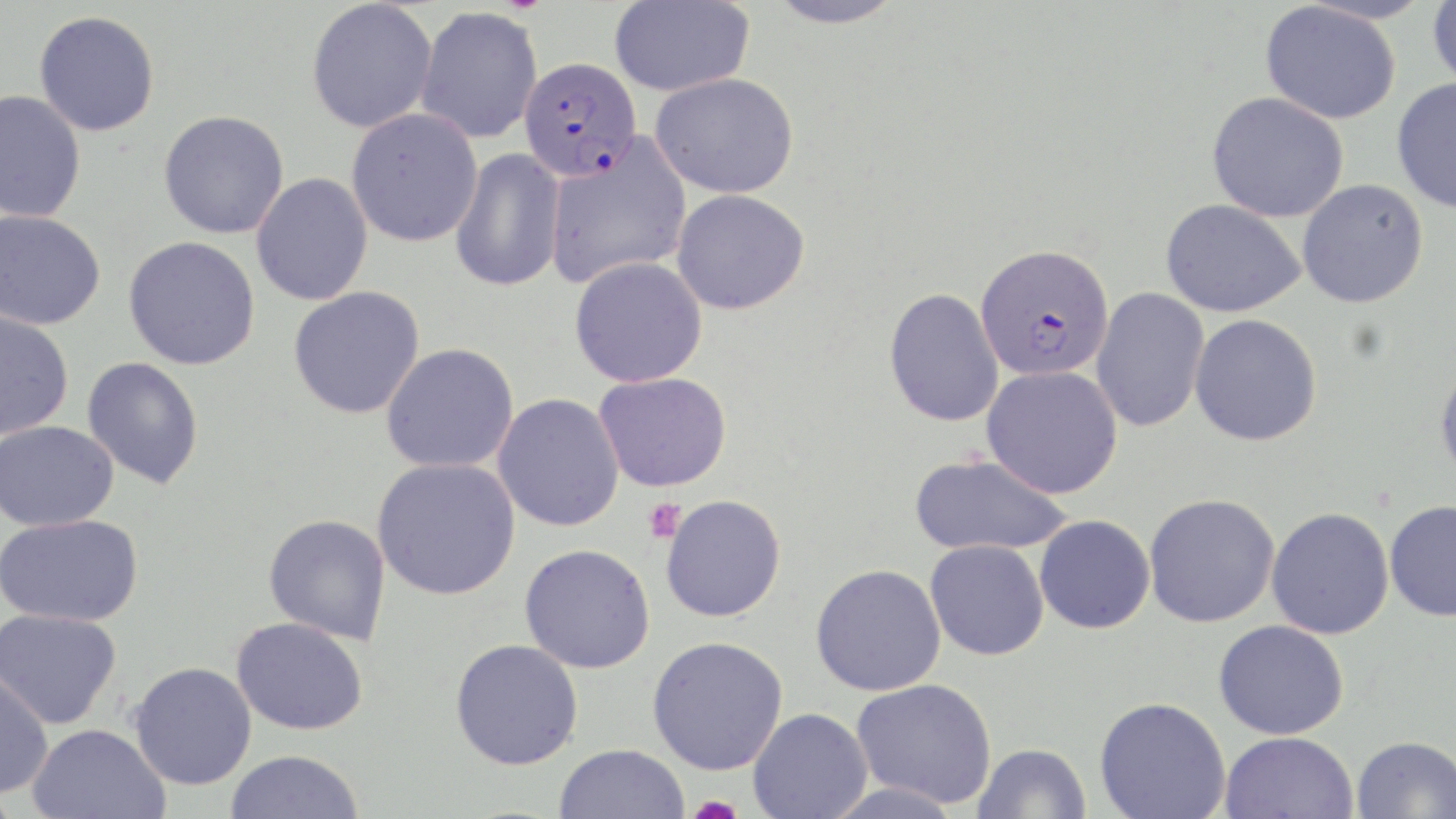 Approximate bounding boxes as named x1/y1/x2/y2 corners in pixels. Plasmodium falciparum-infected red blood cell locations: (x1=518, y1=56, x2=641, y2=181), (x1=975, y1=243, x2=1114, y2=381). Platelet locations: (x1=643, y1=498, x2=687, y2=543), (x1=684, y1=796, x2=746, y2=819). Uninfected red blood cell locations: (x1=306, y1=0, x2=438, y2=133), (x1=609, y1=0, x2=754, y2=96), (x1=764, y1=0, x2=907, y2=29), (x1=1427, y1=0, x2=1456, y2=93), (x1=1260, y1=2, x2=1401, y2=124), (x1=415, y1=6, x2=543, y2=144), (x1=33, y1=10, x2=160, y2=137), (x1=650, y1=72, x2=800, y2=198), (x1=1392, y1=77, x2=1456, y2=215), (x1=0, y1=90, x2=86, y2=222), (x1=1207, y1=92, x2=1349, y2=222), (x1=158, y1=109, x2=289, y2=239), (x1=346, y1=109, x2=483, y2=247), (x1=544, y1=136, x2=692, y2=289), (x1=449, y1=147, x2=566, y2=293), (x1=251, y1=173, x2=373, y2=306), (x1=1297, y1=178, x2=1429, y2=308), (x1=671, y1=189, x2=810, y2=315), (x1=1160, y1=199, x2=1306, y2=317), (x1=0, y1=210, x2=105, y2=330), (x1=122, y1=236, x2=261, y2=371), (x1=569, y1=257, x2=708, y2=387), (x1=288, y1=286, x2=426, y2=419), (x1=883, y1=287, x2=1004, y2=427), (x1=1091, y1=287, x2=1210, y2=433), (x1=0, y1=309, x2=74, y2=439), (x1=1189, y1=313, x2=1322, y2=446), (x1=381, y1=343, x2=519, y2=474), (x1=82, y1=356, x2=205, y2=490), (x1=1434, y1=360, x2=1456, y2=486), (x1=981, y1=365, x2=1123, y2=498), (x1=593, y1=371, x2=732, y2=492), (x1=492, y1=393, x2=625, y2=532), (x1=0, y1=421, x2=118, y2=531), (x1=908, y1=453, x2=1072, y2=557), (x1=372, y1=457, x2=520, y2=600), (x1=1143, y1=493, x2=1280, y2=628), (x1=660, y1=494, x2=786, y2=623), (x1=1384, y1=499, x2=1456, y2=622), (x1=1265, y1=507, x2=1394, y2=639), (x1=1, y1=513, x2=144, y2=627), (x1=263, y1=513, x2=391, y2=645), (x1=1034, y1=514, x2=1156, y2=634), (x1=924, y1=539, x2=1049, y2=661), (x1=519, y1=543, x2=655, y2=673), (x1=810, y1=564, x2=947, y2=697), (x1=0, y1=608, x2=122, y2=729), (x1=231, y1=616, x2=369, y2=735), (x1=1212, y1=619, x2=1349, y2=740), (x1=647, y1=636, x2=789, y2=775), (x1=449, y1=639, x2=584, y2=771), (x1=129, y1=661, x2=257, y2=790), (x1=0, y1=669, x2=53, y2=798), (x1=851, y1=678, x2=997, y2=808), (x1=1094, y1=696, x2=1231, y2=819), (x1=747, y1=707, x2=872, y2=819), (x1=27, y1=723, x2=170, y2=819), (x1=1220, y1=731, x2=1358, y2=819), (x1=1351, y1=735, x2=1456, y2=819), (x1=973, y1=742, x2=1091, y2=819), (x1=554, y1=744, x2=689, y2=819), (x1=225, y1=750, x2=365, y2=819). Slide-level diagnosis: Plasmodium falciparum. May-Grünwald-Giemsa-stained preparation. Optical microscopy. One field of a larger specimen. Captured at 1000x magnification. Image is 1456×819 pixels. Thin blood smear.